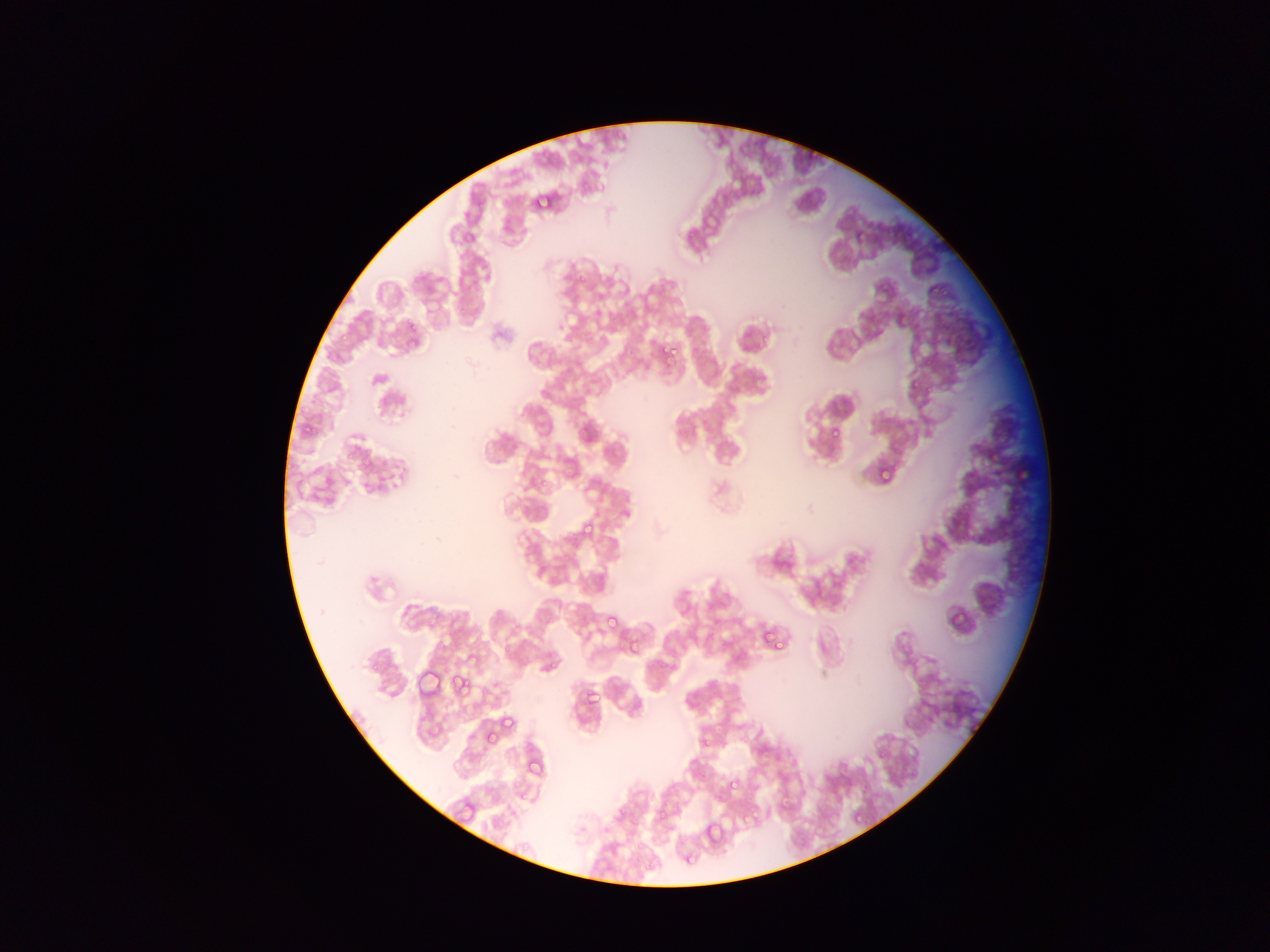 Approximate bounding boxes as left top right bottom in pixels. Plasmodium parasite locations: 536 194 551 207; 898 316 907 322; 409 324 418 332; 408 341 416 349; 665 344 669 354; 669 349 681 354; 664 355 675 364; 924 360 933 367; 911 378 920 390; 831 430 843 436; 989 452 1005 461; 1019 464 1030 480; 882 467 892 480; 582 524 593 532; 950 609 968 623; 606 615 619 630; 764 631 775 639; 630 636 638 653; 776 640 785 651; 453 674 466 689; 587 690 599 704; 485 725 498 742; 704 737 712 746; 730 780 738 789; 781 798 789 806; 855 812 863 821; 742 815 750 824; 706 819 724 842 | approximate x y pixel centers of objects too small to bound: 935 291; 408 320; 345 338; 524 796; 639 847. Thin blood film. Sample from Ghana. Single field of view. Image is 1270×952 pixels. Mobile-phone photograph taken through the microscope.